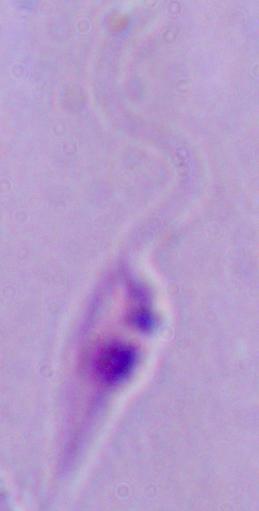 A Leishmania parasite is seen. Photomicrograph. Captured at 1000x magnification.